Outline each Plasmodium falciparum-infected red blood cell.
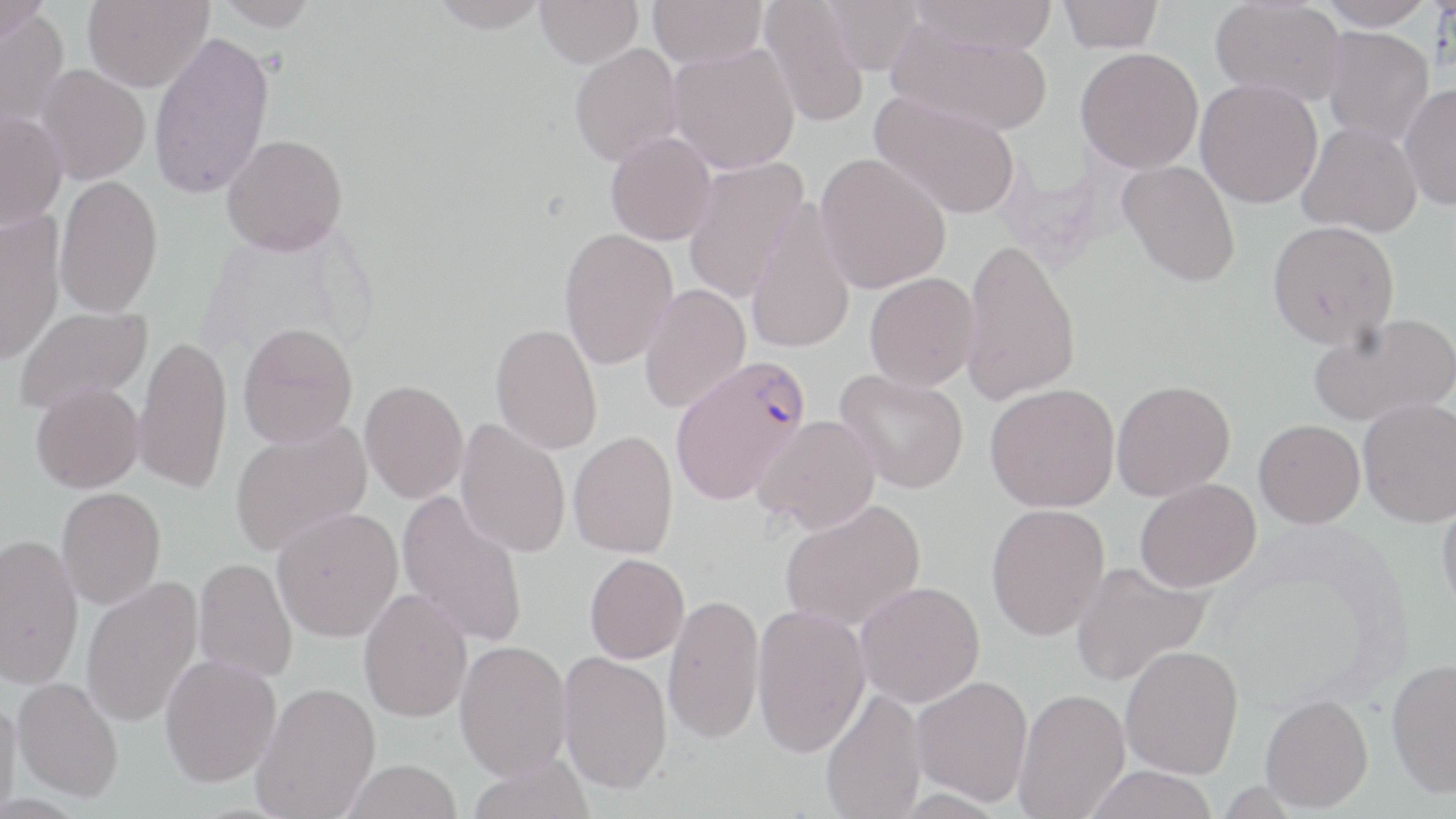

Approximate bounding boxes as (x1, y1, x2, y2) in pixels.
Plasmodium falciparum-infected red blood cells: (669, 354, 812, 506).

Uninfected red blood cell locations: (0, 0, 50, 45), (82, 0, 213, 92), (214, 0, 319, 30), (428, 0, 551, 33), (535, 0, 644, 68), (648, 0, 767, 67), (758, 0, 870, 129), (823, 0, 924, 75), (910, 0, 1059, 56), (1058, 0, 1164, 53), (1210, 0, 1346, 106), (1316, 0, 1437, 30), (0, 9, 69, 135), (885, 17, 1053, 138), (1322, 26, 1434, 147), (148, 30, 275, 200), (569, 43, 683, 166), (668, 43, 800, 174), (1075, 47, 1204, 173), (35, 64, 150, 184), (1196, 78, 1323, 208), (1399, 83, 1456, 211), (869, 93, 1021, 220), (0, 110, 67, 230), (1297, 124, 1422, 237), (605, 132, 716, 245), (221, 134, 348, 255), (815, 152, 951, 293), (682, 157, 809, 302), (1117, 160, 1241, 287), (55, 175, 163, 318), (746, 199, 856, 355), (0, 210, 65, 366), (1267, 220, 1399, 348), (558, 227, 678, 370), (961, 236, 1081, 407), (864, 272, 980, 391), (638, 284, 751, 414), (13, 305, 152, 413), (1308, 313, 1454, 427), (237, 322, 358, 449), (490, 323, 603, 455), (133, 336, 233, 494), (835, 369, 969, 494), (360, 379, 469, 503), (1112, 380, 1235, 501), (30, 381, 144, 493), (985, 383, 1119, 513), (1359, 399, 1456, 527), (753, 415, 881, 533), (455, 419, 571, 558), (1254, 419, 1366, 528), (229, 421, 372, 557), (568, 431, 680, 558), (1135, 478, 1261, 592), (56, 487, 166, 609), (396, 490, 529, 648), (1437, 495, 1456, 618), (779, 499, 926, 632), (986, 503, 1110, 640), (271, 507, 402, 641), (0, 533, 84, 688), (584, 553, 689, 664), (193, 557, 297, 683), (1070, 561, 1211, 687), (80, 578, 203, 727), (855, 581, 985, 707), (358, 587, 472, 722), (663, 593, 765, 744), (751, 604, 871, 757), (454, 640, 573, 780), (1120, 645, 1244, 778), (558, 651, 672, 794), (160, 653, 281, 787), (1385, 658, 1456, 797), (12, 676, 124, 801), (911, 676, 1034, 806), (251, 681, 380, 818), (1013, 687, 1130, 818), (820, 688, 926, 819), (1260, 694, 1373, 812), (0, 695, 23, 818), (467, 754, 594, 819), (339, 758, 463, 819), (1083, 765, 1220, 819). Slide-level diagnosis: Plasmodium falciparum. Optical microscopy. May-Grünwald-Giemsa-stained preparation. One field of a larger specimen. Image is 1456×819 pixels. Thin blood smear. Captured at 1000x magnification.